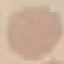
Summary:
  - Result: no malaria parasites seen
  - Preparation: thin blood smear
  - Stain: Giemsa
  - Image type: automatically extracted cell patch, resized to 64 × 64 pixels
  - Capture: smartphone camera at the microscope eyepiece